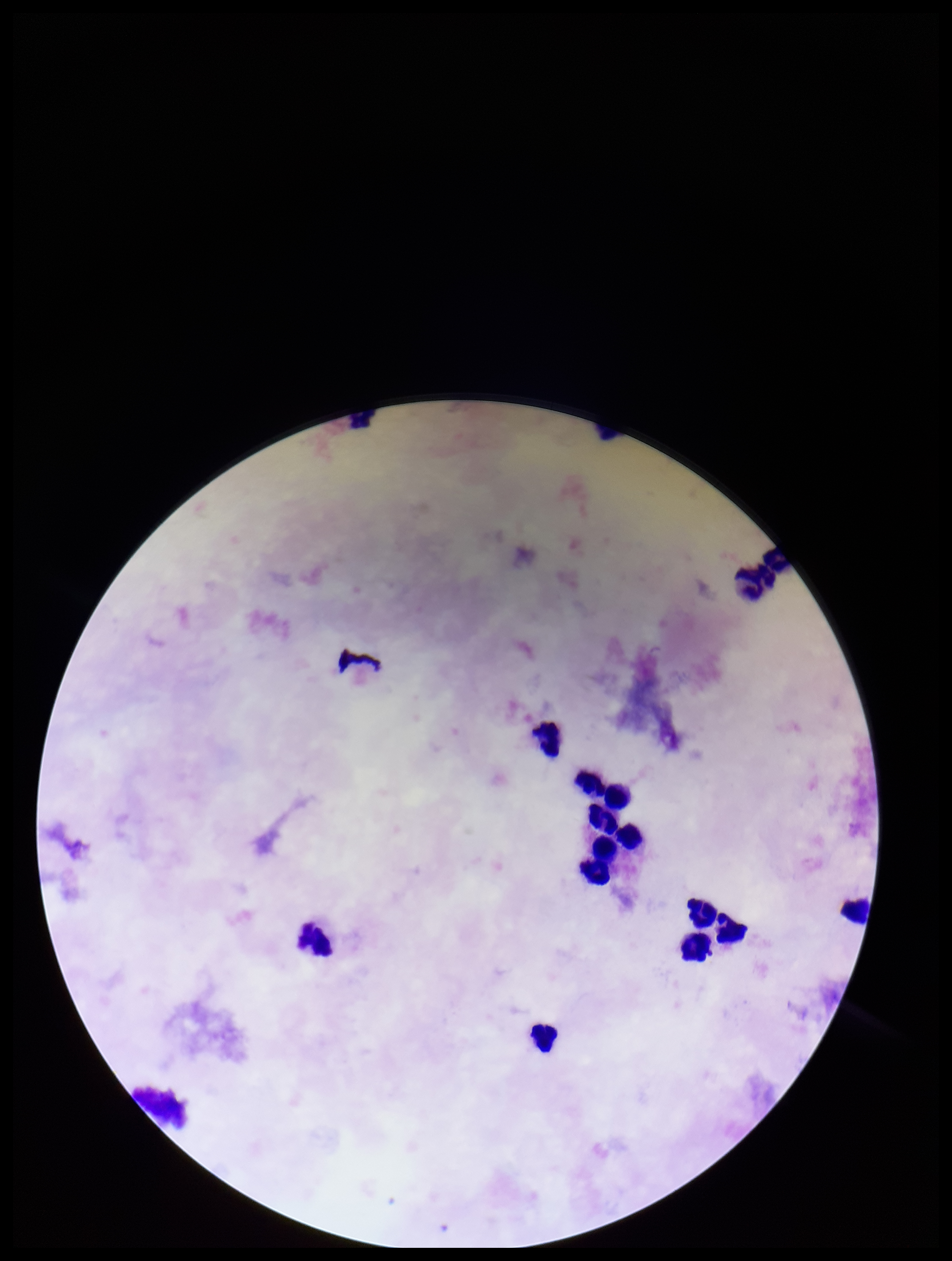

parasite count = 0
leukocyte count = 14
patient malaria status = negative
stain = Giemsa
image size = 952×1261 pixels
preparation = thick smear
capture = smartphone photograph through the microscope eyepiece
Plasmodium parasites = none detected
field of view = one from this slide